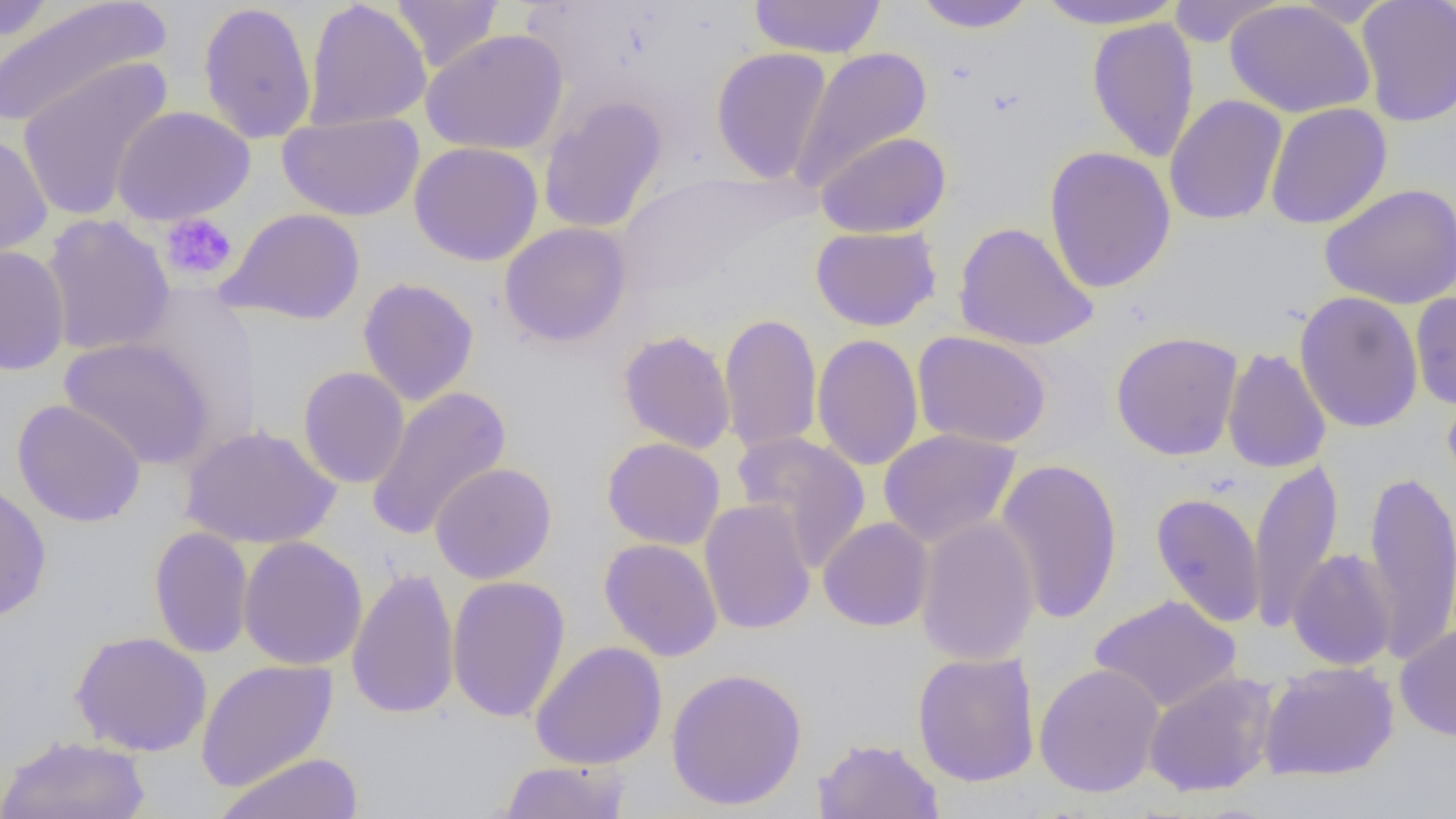

Approximate bounding boxes as [x1, y1, x2, y2] in pixels. Platelet locations: [160, 212, 238, 283]. Uninfected red blood cell locations: [0, 0, 170, 131], [304, 0, 431, 131], [391, 0, 504, 73], [749, 0, 887, 59], [910, 0, 1037, 33], [1033, 0, 1186, 30], [1355, 0, 1456, 126], [0, 1, 59, 42], [197, 1, 317, 145], [1163, 1, 1285, 46], [1224, 1, 1375, 118], [1086, 17, 1200, 162], [422, 28, 569, 156], [711, 47, 833, 184], [791, 47, 933, 191], [14, 57, 174, 223], [537, 95, 668, 234], [1164, 95, 1288, 225], [1265, 102, 1392, 230], [111, 105, 255, 225], [278, 112, 424, 222], [0, 130, 53, 261], [816, 131, 952, 238], [409, 141, 543, 266], [1043, 146, 1177, 294], [1319, 183, 1456, 309], [219, 207, 366, 325], [41, 214, 175, 357], [953, 221, 1098, 351], [499, 222, 633, 348], [810, 226, 941, 331], [0, 244, 70, 376], [357, 277, 479, 406], [1294, 291, 1424, 433], [1410, 292, 1456, 411], [719, 312, 823, 456], [617, 329, 736, 454], [913, 330, 1052, 449], [1110, 331, 1244, 461], [811, 333, 923, 472], [59, 337, 216, 470], [1222, 347, 1331, 474], [297, 366, 410, 489], [366, 386, 512, 541], [12, 399, 146, 528], [180, 423, 341, 550], [878, 428, 1022, 549], [732, 431, 871, 571], [602, 437, 725, 550], [993, 457, 1123, 625], [1248, 458, 1344, 633], [430, 462, 558, 584], [1363, 464, 1456, 666], [0, 479, 52, 623], [1150, 491, 1266, 627], [699, 499, 816, 635], [915, 515, 1040, 666], [818, 517, 934, 631], [148, 527, 254, 659], [238, 535, 368, 671], [598, 538, 723, 661], [1287, 548, 1398, 670], [346, 566, 460, 719], [447, 575, 571, 723], [1089, 594, 1242, 714], [1395, 624, 1456, 742], [69, 631, 212, 757], [530, 640, 668, 770], [912, 651, 1041, 787], [195, 658, 339, 792], [1259, 661, 1399, 781], [1033, 662, 1165, 798], [666, 667, 807, 811], [1143, 671, 1278, 797], [0, 734, 151, 818], [812, 736, 945, 819], [213, 752, 363, 819], [496, 759, 631, 818]. Slide-level diagnosis: no evidence of blood parasites. Light microscopy. Image is 1456×819 pixels. Thin blood film. Captured at 1000x magnification. Single field of view.